Locate and identify every blood parasite.
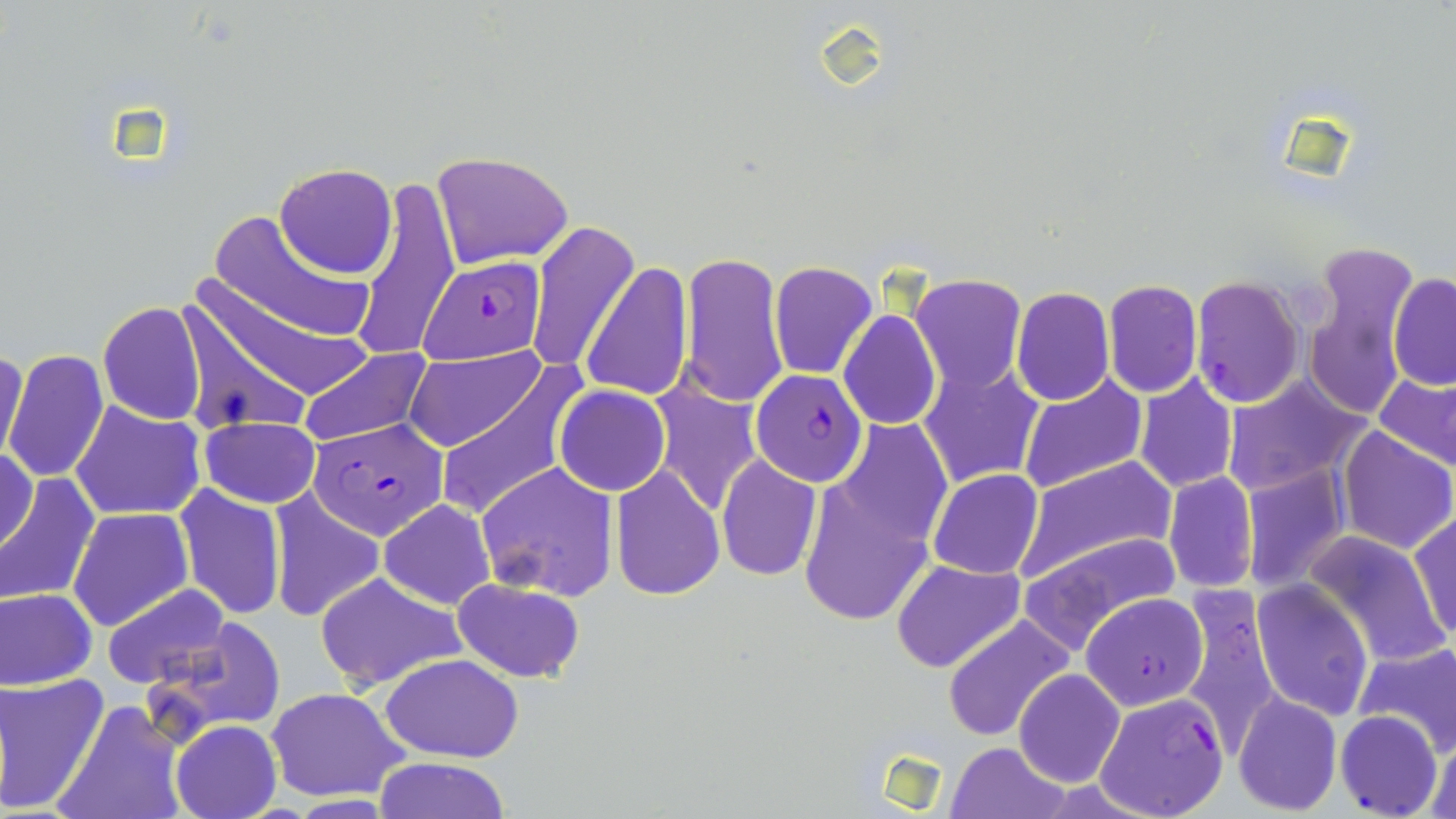

Approximate bounding boxes as (x1,y1)-(x2,y2) corner pairs in pixels.
Plasmodium falciparum-infected red blood cells: (417,256)-(547,364), (1190,275)-(1306,408), (751,370)-(868,486), (312,418)-(449,539), (1177,588)-(1284,751), (1082,592)-(1209,710), (1095,692)-(1228,819), (1335,710)-(1441,818).
No Plasmodium ovale, Plasmodium malariae, Plasmodium vivax, Babesia divergens, or Trypanosoma brucei observed.

slide-level diagnosis = Plasmodium falciparum
preparation = thin blood film
field of view = one of a larger specimen
image size = 1456×819 pixels
magnification = 1000x
stain = May-Grünwald-Giemsa
uninfected red blood cell locations = approximate bounding boxes as (x1,y1)-(x2,y2) corner pairs in pixels: (429,151)-(573,269), (274,163)-(397,279), (352,179)-(461,364), (207,208)-(378,349), (525,219)-(638,375), (1300,247)-(1417,414), (681,251)-(790,408), (769,261)-(878,380), (581,262)-(692,402), (1388,273)-(1456,390), (178,276)-(362,426), (911,276)-(1027,392), (1102,278)-(1203,399), (1012,286)-(1114,404), (97,301)-(208,426), (837,310)-(941,430), (0,343)-(27,471), (296,347)-(433,450), (409,348)-(546,452), (3,349)-(111,485), (918,361)-(1044,489), (428,363)-(584,519), (1375,374)-(1454,467), (1018,375)-(1148,494), (1133,375)-(1238,493), (1222,375)-(1368,494), (650,381)-(763,516), (555,384)-(670,496), (70,401)-(207,522), (199,415)-(323,509), (833,419)-(952,551), (1334,425)-(1455,554), (1246,444)-(1448,575), (0,446)-(38,559), (716,453)-(822,581), (1015,456)-(1177,582), (476,461)-(620,602), (1239,464)-(1349,593), (609,467)-(725,598), (928,469)-(1044,579), (796,470)-(937,630), (0,472)-(98,608), (1161,473)-(1259,592), (173,483)-(285,621), (270,491)-(385,622), (379,498)-(497,609), (67,508)-(194,631), (1408,510)-(1456,643), (1022,530)-(1182,645), (1302,530)-(1450,667), (891,559)-(1024,673), (312,572)-(464,691), (452,578)-(584,682), (1249,580)-(1375,720), (100,584)-(232,691), (1,586)-(99,690), (941,614)-(1073,741), (160,615)-(285,732), (1353,640)-(1456,754), (382,653)-(524,760), (1013,668)-(1125,788), (1,671)-(110,816), (265,686)-(409,802), (1233,691)-(1343,812), (53,700)-(188,819), (170,719)-(282,819), (1424,729)-(1455,819), (946,740)-(1069,819), (374,757)-(511,817)
modality = optical microscopy